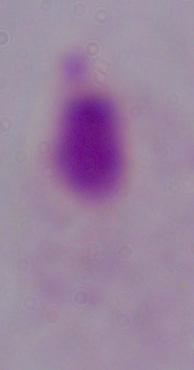
{
  "modality": "photomicrograph",
  "identification": "trichomonad",
  "magnification": "1000x"
}